State the blood parasite species.
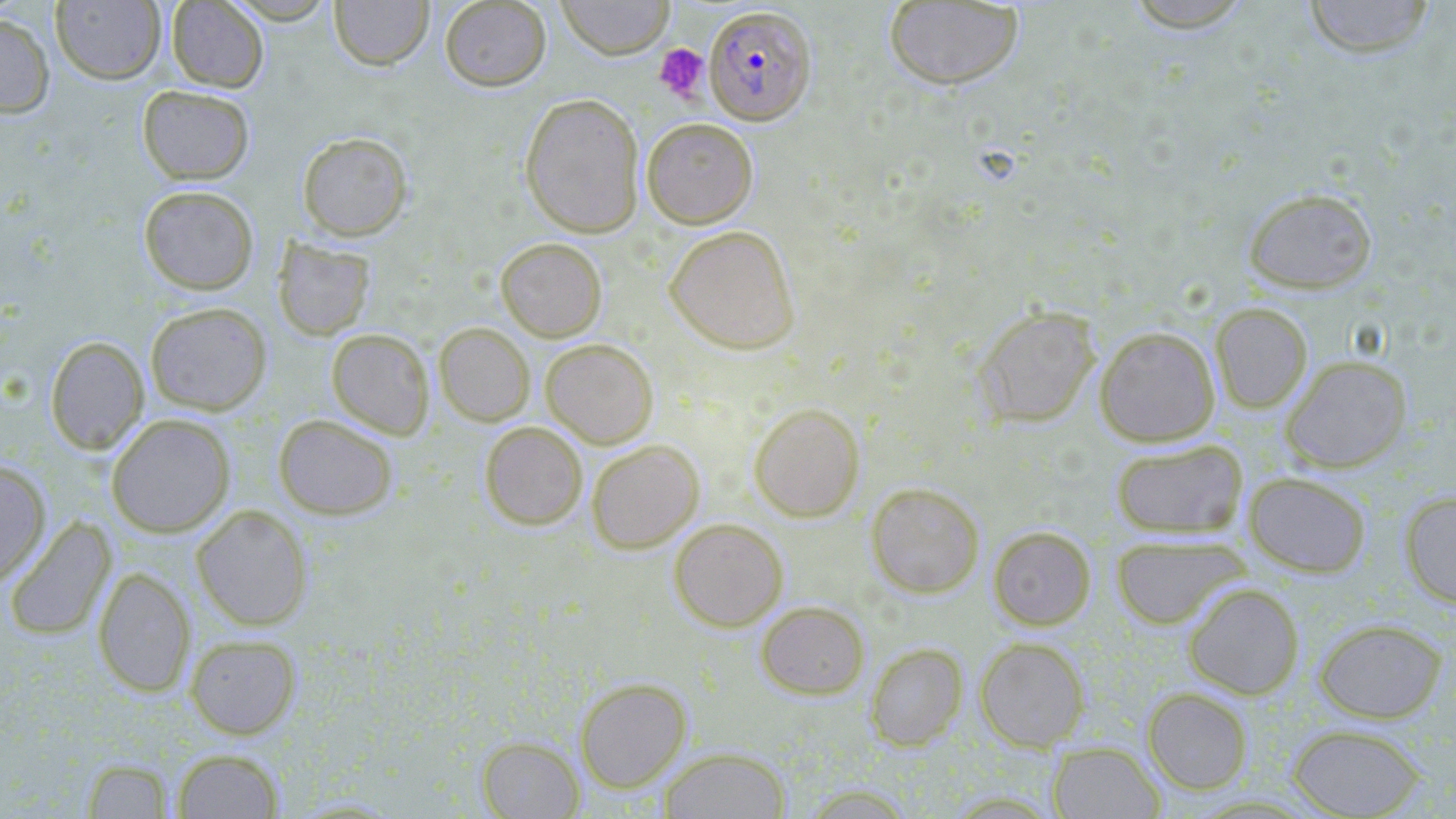
Plasmodium falciparum.

Approximate bounding boxes as [x1, y1, x2, y2] in pixels. Platelet locations: [654, 43, 710, 102]. Plasmodium falciparum-infected red blood cell locations: [704, 4, 816, 125]. Uninfected red blood cell locations: [51, 0, 166, 85], [166, 0, 268, 92], [222, 0, 340, 24], [329, 0, 434, 70], [439, 0, 551, 91], [556, 0, 674, 59], [1123, 0, 1256, 33], [1303, 0, 1436, 59], [884, 1, 1024, 90], [0, 13, 55, 118], [137, 85, 255, 184], [520, 92, 645, 237], [641, 117, 758, 229], [297, 131, 413, 241], [138, 185, 259, 295], [1243, 187, 1377, 294], [664, 224, 800, 354], [273, 237, 375, 341], [495, 237, 607, 342], [145, 301, 272, 415], [1210, 303, 1313, 413], [973, 305, 1101, 427], [434, 322, 535, 426], [1095, 326, 1220, 447], [326, 328, 435, 439], [45, 335, 148, 454], [540, 338, 658, 448], [1280, 355, 1412, 473], [749, 401, 865, 522], [106, 414, 235, 537], [273, 414, 398, 519], [479, 421, 588, 530], [586, 439, 704, 553], [1110, 439, 1248, 539], [0, 460, 50, 587], [1244, 472, 1372, 578], [866, 482, 985, 598], [1399, 490, 1456, 608], [192, 504, 313, 631], [4, 516, 117, 641], [668, 517, 787, 631], [988, 525, 1096, 630], [1109, 534, 1249, 629], [93, 567, 195, 697], [1183, 582, 1304, 699], [756, 600, 869, 699], [1300, 618, 1432, 817], [1314, 618, 1447, 723], [185, 634, 301, 739], [975, 637, 1089, 751], [865, 642, 968, 750], [575, 677, 692, 792], [1142, 687, 1253, 794], [1287, 723, 1426, 818], [476, 736, 584, 818], [1048, 741, 1165, 818], [659, 746, 791, 818], [171, 748, 284, 818], [82, 758, 174, 819]. One field of a larger specimen. Thin blood film. Captured at 1000x magnification. May-Grünwald-Giemsa stain. Light microscopy. Image is 1456×819 pixels.